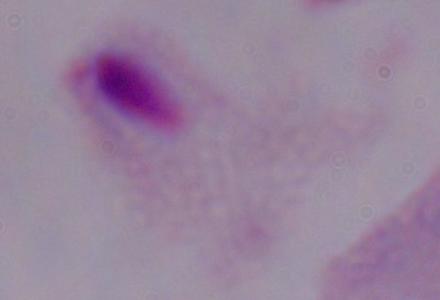

Micrograph. 1000x magnification. A trichomonad is shown.